Give the position of every Plasmodium parasite.
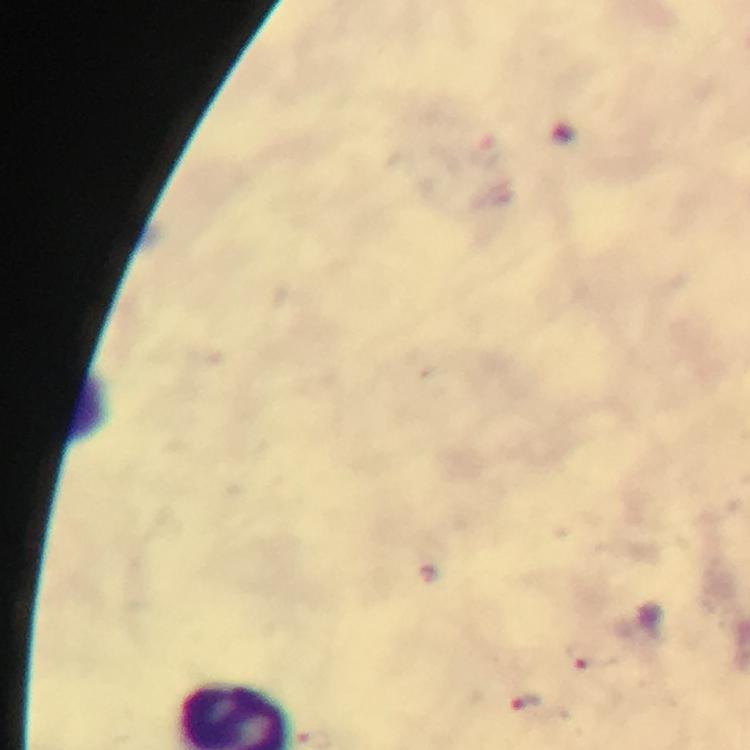

Approximate centers as [x, y] in pixels.
Plasmodium parasites: [582, 656], [526, 704].

Cropped region of a single field of view. Immersion oil applied. From a malaria diagnostic workup. Giemsa-stained preparation. Image is 750×750 pixels. 100x magnification. Thick smear. Photographed through the microscope with a smartphone camera.